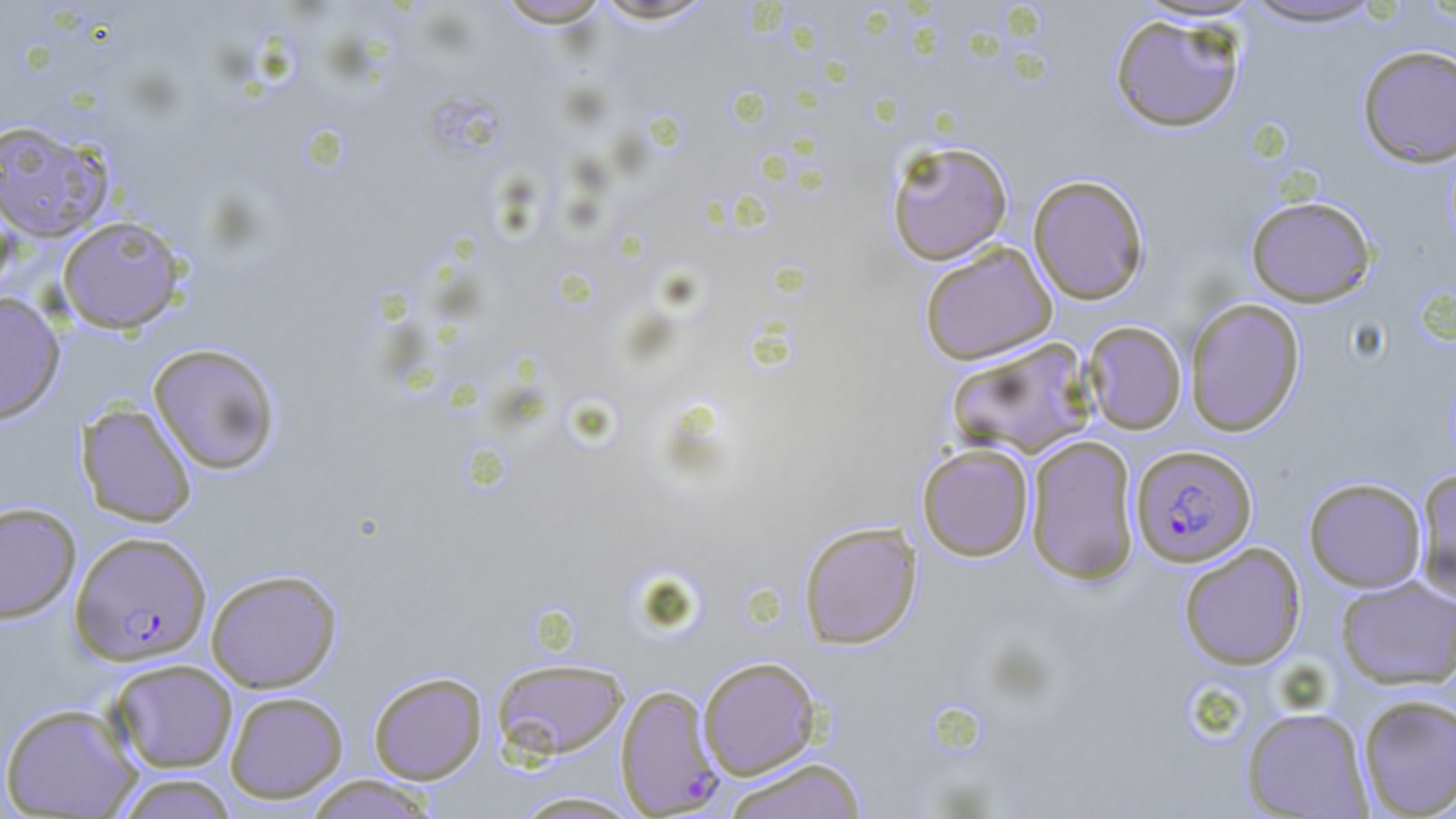

slide-level diagnosis = Plasmodium falciparum
image size = 1456×819 pixels
uninfected red blood cell locations = approximate bounding boxes as named x1/y1/x2/y2 corners in pixels: (x1=586, y1=0, x2=722, y2=25), (x1=493, y1=1, x2=614, y2=28), (x1=1236, y1=1, x2=1389, y2=29), (x1=1109, y1=14, x2=1245, y2=133), (x1=1356, y1=44, x2=1456, y2=167), (x1=0, y1=119, x2=114, y2=242), (x1=886, y1=140, x2=1013, y2=265), (x1=1028, y1=174, x2=1149, y2=305), (x1=1245, y1=196, x2=1376, y2=307), (x1=0, y1=199, x2=17, y2=303), (x1=57, y1=215, x2=187, y2=333), (x1=919, y1=242, x2=1058, y2=365), (x1=0, y1=292, x2=65, y2=425), (x1=1184, y1=298, x2=1305, y2=436), (x1=1082, y1=321, x2=1187, y2=434), (x1=945, y1=337, x2=1097, y2=459), (x1=148, y1=342, x2=281, y2=474), (x1=76, y1=403, x2=197, y2=527), (x1=1025, y1=435, x2=1140, y2=584), (x1=917, y1=442, x2=1035, y2=561), (x1=1414, y1=468, x2=1456, y2=603), (x1=1303, y1=477, x2=1427, y2=593), (x1=0, y1=502, x2=81, y2=623), (x1=798, y1=521, x2=922, y2=649), (x1=1178, y1=542, x2=1307, y2=671), (x1=206, y1=569, x2=342, y2=693), (x1=1335, y1=575, x2=1456, y2=690), (x1=697, y1=656, x2=822, y2=780), (x1=492, y1=658, x2=629, y2=760), (x1=108, y1=659, x2=238, y2=773), (x1=368, y1=671, x2=487, y2=784), (x1=225, y1=691, x2=348, y2=803), (x1=1357, y1=694, x2=1456, y2=817), (x1=0, y1=702, x2=142, y2=818), (x1=1241, y1=705, x2=1373, y2=818), (x1=720, y1=757, x2=869, y2=819), (x1=113, y1=773, x2=239, y2=818), (x1=301, y1=775, x2=440, y2=818), (x1=508, y1=790, x2=647, y2=818)
preparation = thin blood smear
magnification = 1000x
Plasmodium falciparum-infected red blood cell locations = approximate bounding boxes as named x1/y1/x2/y2 corners in pixels: (x1=1130, y1=444, x2=1257, y2=566), (x1=70, y1=531, x2=211, y2=665), (x1=615, y1=684, x2=725, y2=816)
stain = May-Grünwald-Giemsa
modality = optical microscopy
field of view = single